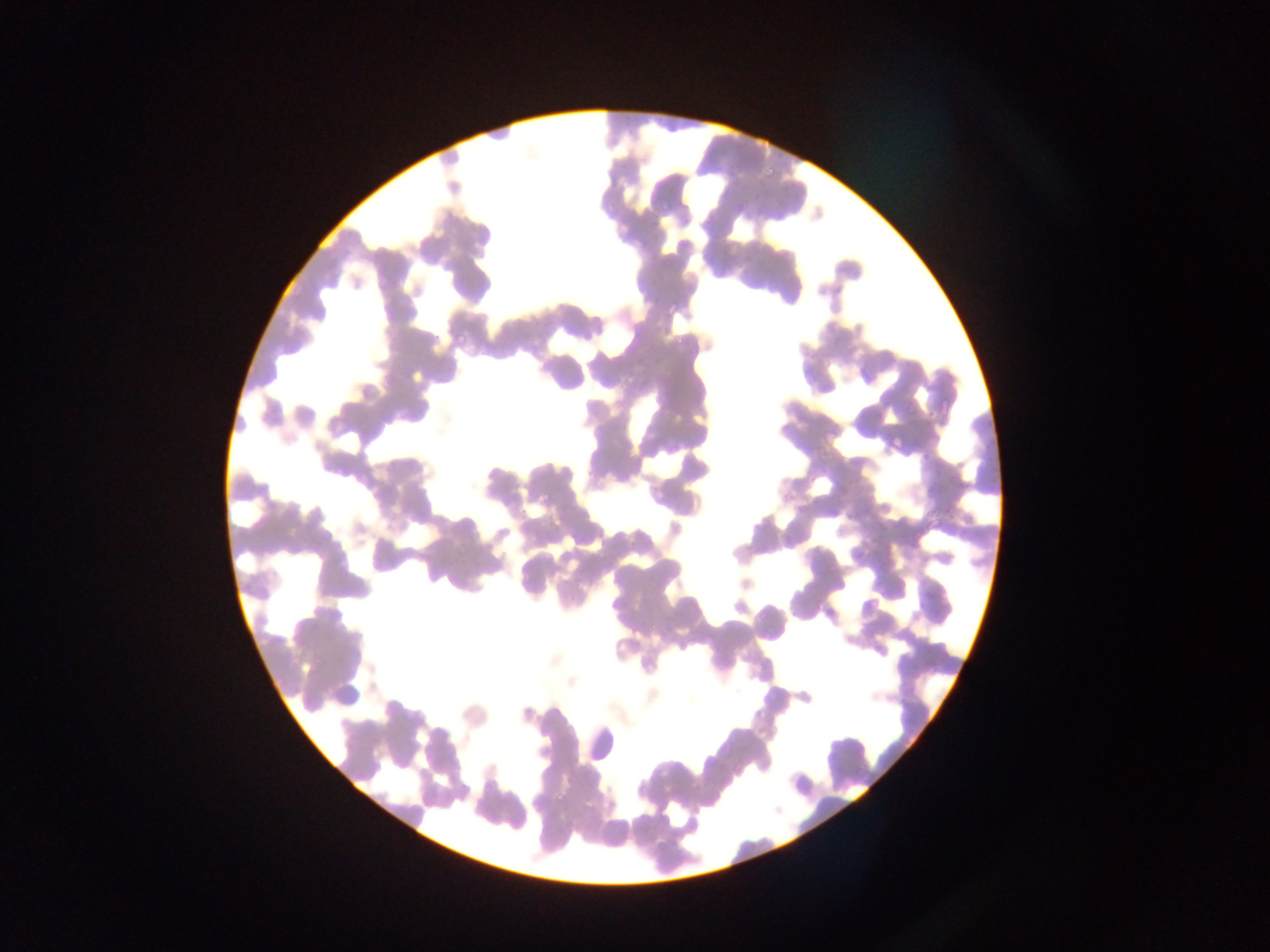
Approximate bounding boxes as [left, top, right, bottom] in pixels.
Summary:
  - Leukocyte locations: [578, 721, 621, 763]
  - Plasmodium parasite locations: [760, 165, 776, 182], [601, 203, 613, 217], [769, 209, 787, 226], [665, 303, 680, 319], [451, 328, 467, 346], [671, 334, 689, 352], [887, 434, 906, 454], [924, 517, 945, 533], [451, 542, 467, 558], [552, 792, 568, 809]
  - Country: Ghana
  - Field of view: single
  - Image size: 1270×952 pixels
  - Capture: mobile-phone photograph through a microscope
  - Preparation: thin blood film